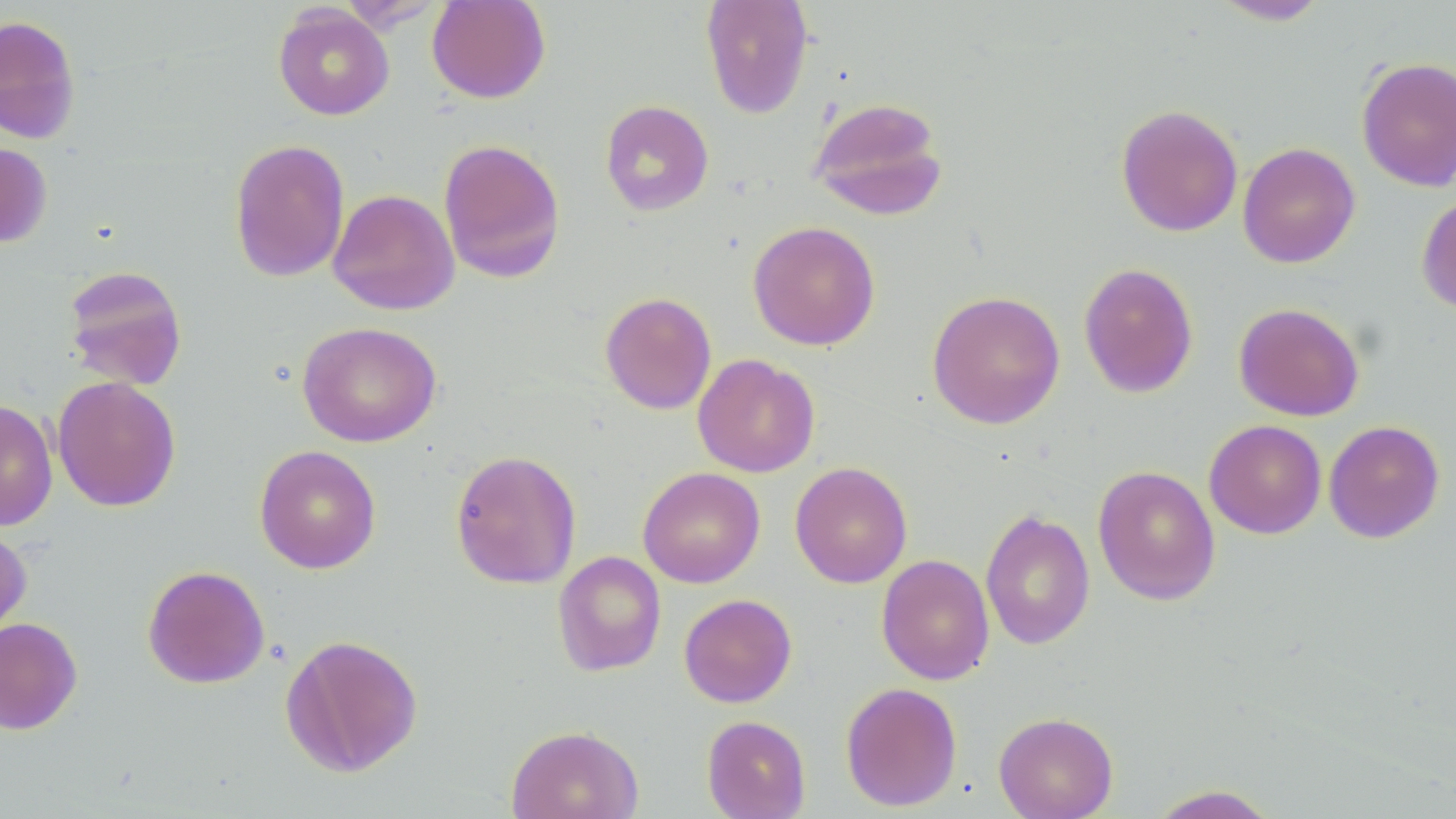 Approximate bounding boxes as (x1, y1, x2, y2) in pixels. Uninfected red blood cell locations: (426, 0, 550, 104), (700, 0, 814, 119), (1211, 0, 1330, 26), (273, 4, 394, 120), (0, 15, 81, 144), (1356, 56, 1456, 192), (807, 96, 949, 221), (600, 99, 714, 216), (1115, 103, 1243, 238), (229, 138, 350, 283), (438, 138, 566, 283), (0, 142, 52, 247), (1237, 142, 1361, 268), (328, 189, 460, 316), (1416, 192, 1456, 316), (748, 221, 881, 350), (1078, 262, 1199, 399), (63, 265, 188, 390), (927, 290, 1066, 429), (600, 291, 717, 415), (1233, 301, 1365, 421), (296, 321, 442, 447), (693, 353, 820, 478), (52, 376, 181, 512), (0, 399, 58, 531), (1204, 419, 1327, 539), (1323, 420, 1445, 544), (254, 445, 381, 573), (450, 449, 582, 590), (789, 461, 912, 588), (1093, 465, 1221, 606), (637, 467, 765, 588), (980, 508, 1096, 650), (0, 524, 32, 643), (552, 550, 667, 677), (876, 554, 995, 685), (142, 564, 270, 689), (679, 593, 797, 708), (0, 616, 83, 735), (280, 632, 423, 777), (840, 682, 962, 812), (994, 711, 1118, 819), (701, 715, 811, 818), (506, 724, 644, 819), (1144, 784, 1282, 818). Slide-level diagnosis: negative for blood parasites. Thin blood film. Image is 1456×819 pixels. Single field of view. May-Grünwald-Giemsa-stained preparation. Optical microscopy. Captured at 1000x magnification.